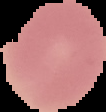
Summary:
  - Preparation: thin blood smear
  - Image type: segmented cell region on a black background
  - Image size: 106×112 pixels
  - Malaria status: uninfected